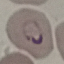

result: malaria parasites identified
image_type: cell patch, automatically extracted from a larger field of view and resized to 64 × 64 pixels
preparation: thin blood smear
capture: smartphone through the microscope eyepiece
stain: Giemsa